Give the position of every leukocyte.
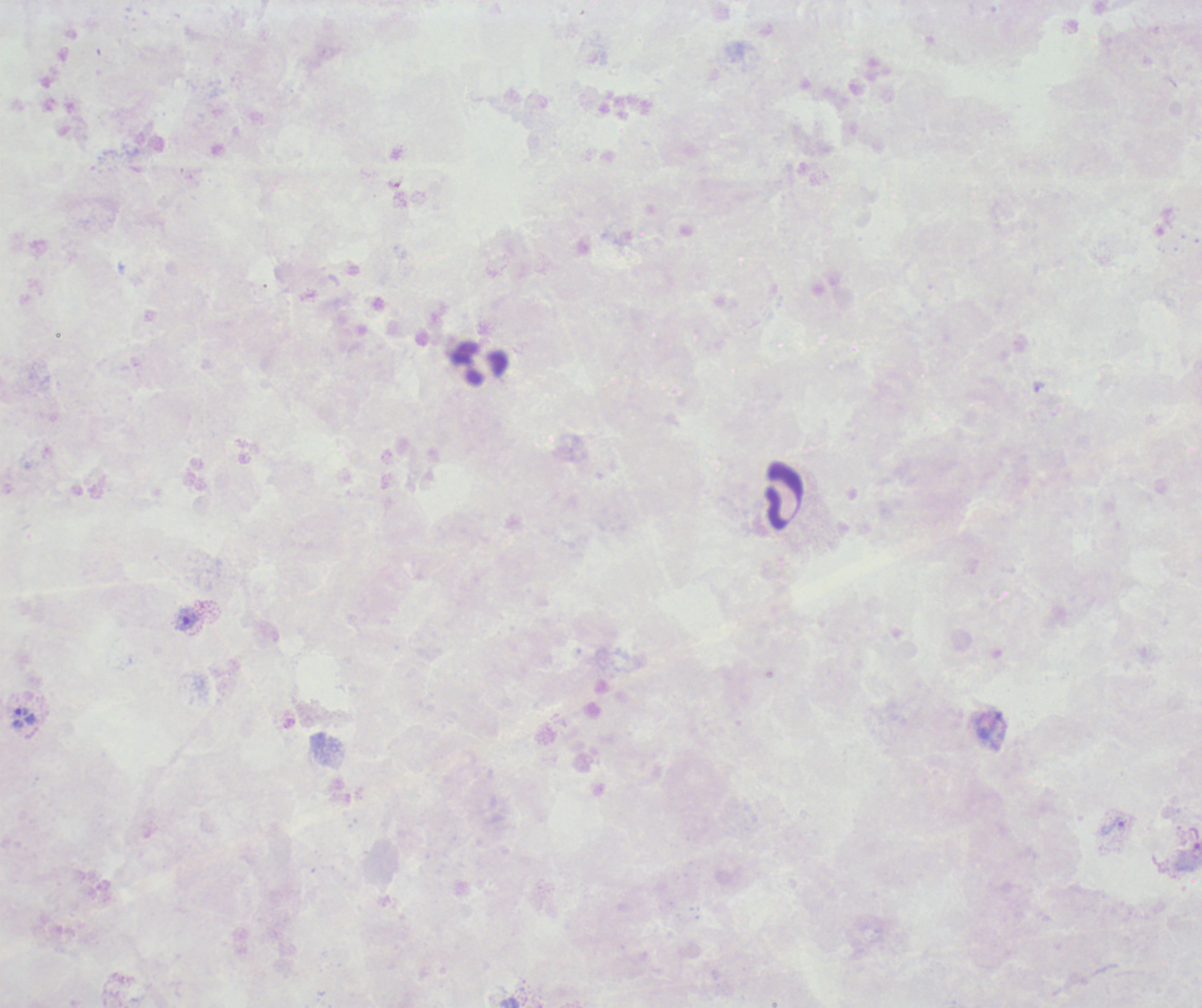
Approximate centers as [x, y] in pixels.
Leukocytes: [481, 363], [782, 495].

coordinate format = approximate centers as [x, y] in pixels
trophozoite locations = [1039, 387], [186, 620], [22, 711], [1113, 825]
result = malaria parasites detected
magnification = 100x
context = previously used in an actual diagnosis
stain = Romanowsky
background quality = poor
image size = 1202×1008 pixels
coloration quality = bad
preparation = thick smear of blood
field of view = one from this slide